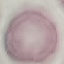
malaria_status: uninfected
stain: Giemsa
capture: smartphone through the microscope eyepiece
preparation: thin blood film
image_type: cell patch, automatically extracted from a larger field of view and resized to 64 × 64 pixels